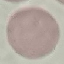
{
  "malaria_status": "uninfected",
  "capture": "smartphone camera at the microscope eyepiece",
  "preparation": "thin blood film",
  "image_type": "cell patch, automatically extracted from a larger field of view and resized to 64 × 64 pixels",
  "stain": "Giemsa"
}